Report the malaria status of this cell.
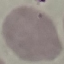

It is uninfected.

Giemsa stain. Automatically extracted cell patch, resized to 64 × 64 pixels. Thin blood smear. Photographed with a smartphone camera at the microscope eyepiece.